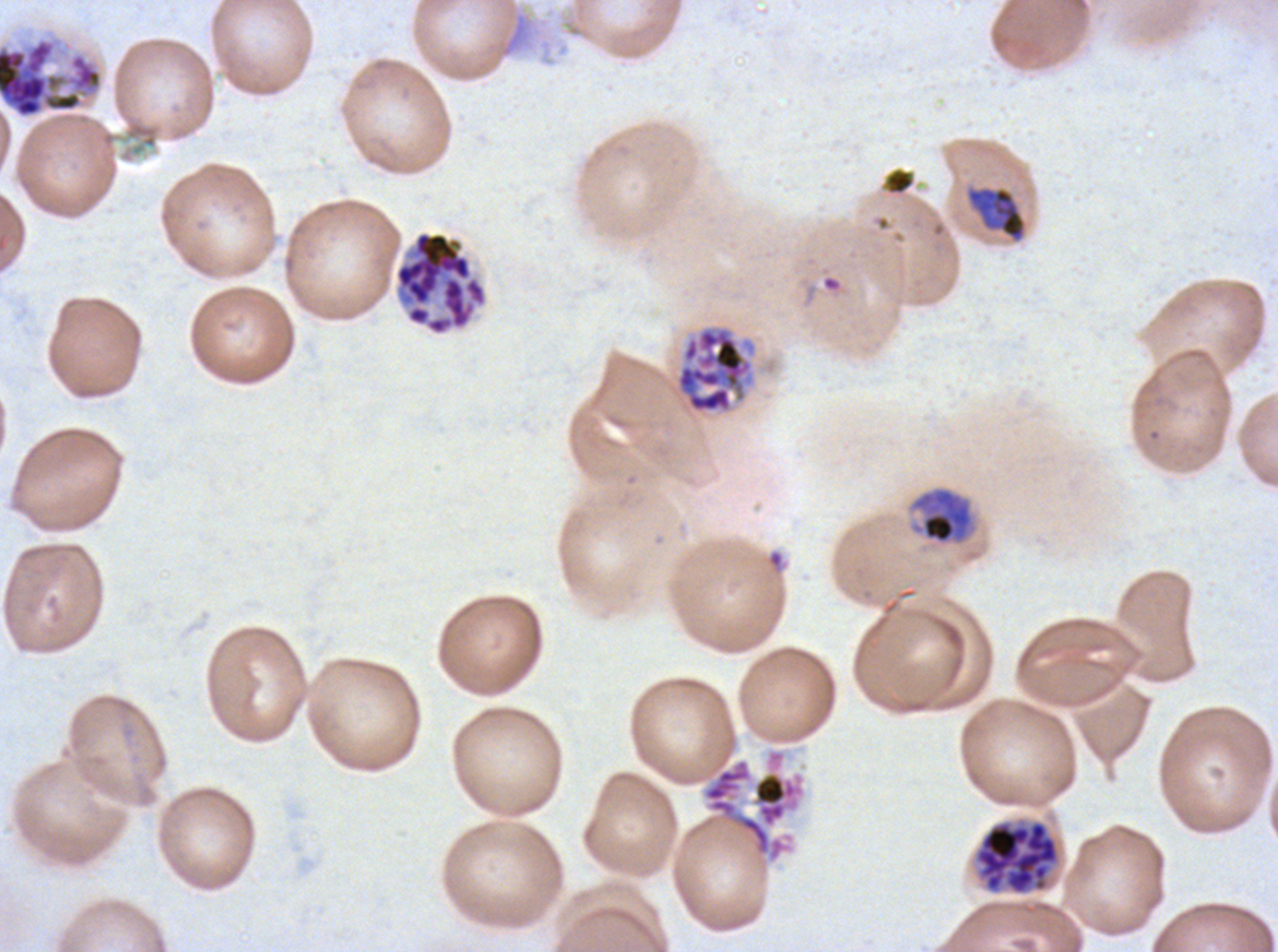

Approximate bounding rectangles given as corner coordinates in pixels from the top-left. Late trophozoite locations: (x1=909, y1=486, x2=976, y2=545). Late schizont locations: (x1=0, y1=36, x2=104, y2=119), (x1=394, y1=230, x2=487, y2=336), (x1=703, y1=758, x2=804, y2=861), (x1=976, y1=821, x2=1059, y2=895). Debris locations: (x1=498, y1=12, x2=531, y2=58), (x1=884, y1=168, x2=915, y2=195). Early schizont locations: (x1=966, y1=186, x2=1026, y2=242), (x1=674, y1=323, x2=758, y2=415). Life-cycle stages observed: late trophozoite, early schizont, late schizont. Giemsa stain. Image is 1278×952 pixels. One sub-image of a larger composite. Thin blood film. Plasmodium falciparum from a patient in The Gambia, cultured ex vivo for 24 to 48 hours.